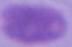
modality = micrograph
magnification = 1000x
identification = erythrocyte